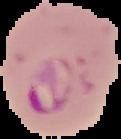

image type = cell region segmented out of the field of view; surrounding area masked to black
preparation = thin blood smear
result = malaria parasites detected
image size = 121×139 pixels